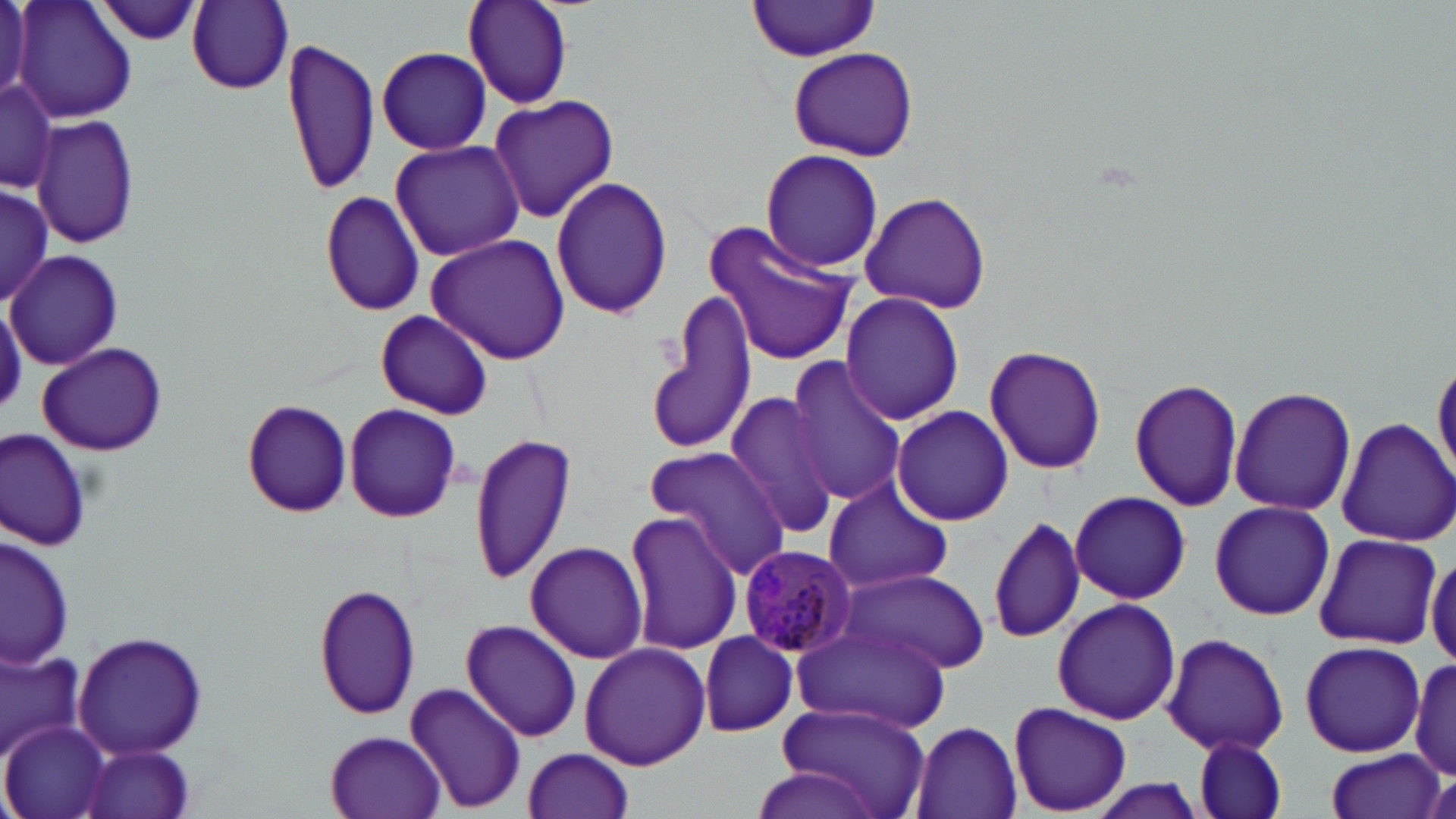

Summary:
  - Coordinate format: approximate bounding boxes as named x1/y1/x2/y2 corners in pixels
  - Uninfected red blood cell locations: (x1=1, y1=0, x2=32, y2=104), (x1=13, y1=0, x2=139, y2=124), (x1=187, y1=1, x2=294, y2=94), (x1=462, y1=1, x2=573, y2=108), (x1=92, y1=2, x2=208, y2=45), (x1=746, y1=2, x2=882, y2=60), (x1=281, y1=35, x2=382, y2=198), (x1=377, y1=47, x2=492, y2=155), (x1=787, y1=47, x2=918, y2=162), (x1=1, y1=72, x2=59, y2=200), (x1=487, y1=93, x2=619, y2=223), (x1=32, y1=114, x2=139, y2=251), (x1=389, y1=139, x2=525, y2=263), (x1=759, y1=148, x2=884, y2=274), (x1=550, y1=174, x2=673, y2=323), (x1=1, y1=186, x2=53, y2=306), (x1=319, y1=189, x2=427, y2=317), (x1=858, y1=190, x2=992, y2=315), (x1=703, y1=221, x2=859, y2=368), (x1=424, y1=232, x2=572, y2=365), (x1=8, y1=251, x2=120, y2=370), (x1=647, y1=289, x2=759, y2=457), (x1=840, y1=291, x2=963, y2=427), (x1=375, y1=310, x2=492, y2=420), (x1=37, y1=341, x2=168, y2=458), (x1=984, y1=344, x2=1106, y2=475), (x1=1431, y1=356, x2=1456, y2=486), (x1=787, y1=358, x2=907, y2=507), (x1=1130, y1=377, x2=1244, y2=512), (x1=1229, y1=385, x2=1357, y2=516), (x1=724, y1=390, x2=843, y2=543), (x1=240, y1=398, x2=355, y2=518), (x1=344, y1=403, x2=463, y2=524), (x1=891, y1=406, x2=1015, y2=526), (x1=1336, y1=418, x2=1456, y2=547), (x1=2, y1=429, x2=94, y2=550), (x1=468, y1=433, x2=579, y2=585), (x1=642, y1=445, x2=790, y2=577), (x1=823, y1=479, x2=953, y2=595), (x1=1069, y1=489, x2=1191, y2=604), (x1=1209, y1=500, x2=1336, y2=621), (x1=624, y1=509, x2=743, y2=655), (x1=988, y1=515, x2=1087, y2=645), (x1=2, y1=533, x2=75, y2=671), (x1=1311, y1=533, x2=1441, y2=651), (x1=523, y1=540, x2=651, y2=664), (x1=1426, y1=548, x2=1456, y2=668), (x1=838, y1=566, x2=989, y2=673), (x1=315, y1=583, x2=423, y2=723), (x1=1050, y1=597, x2=1181, y2=725), (x1=460, y1=617, x2=583, y2=742), (x1=789, y1=621, x2=950, y2=731), (x1=1161, y1=630, x2=1291, y2=757), (x1=73, y1=631, x2=209, y2=759), (x1=699, y1=632, x2=799, y2=737), (x1=1301, y1=641, x2=1426, y2=756), (x1=579, y1=642, x2=710, y2=770), (x1=0, y1=648, x2=82, y2=755), (x1=1410, y1=656, x2=1455, y2=782), (x1=405, y1=680, x2=526, y2=814), (x1=771, y1=699, x2=927, y2=819), (x1=1008, y1=702, x2=1132, y2=816), (x1=909, y1=719, x2=1022, y2=819), (x1=1, y1=721, x2=111, y2=819), (x1=325, y1=730, x2=447, y2=819), (x1=1192, y1=737, x2=1285, y2=819), (x1=80, y1=743, x2=197, y2=819), (x1=523, y1=747, x2=636, y2=819), (x1=1324, y1=750, x2=1447, y2=819), (x1=751, y1=767, x2=885, y2=818)
  - Plasmodium malariae-infected red blood cell locations: (x1=736, y1=544, x2=858, y2=660)
  - Slide-level diagnosis: Plasmodium malariae
  - Modality: light microscopy
  - Preparation: thin blood smear
  - Magnification: 1000x
  - Field of view: one of a larger specimen
  - Image size: 1456×819 pixels
  - Stain: May-Grünwald-Giemsa